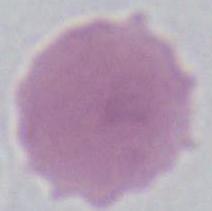
identification = red blood cell
magnification = 1000x
modality = micrograph